Locate every Plasmodium parasite.
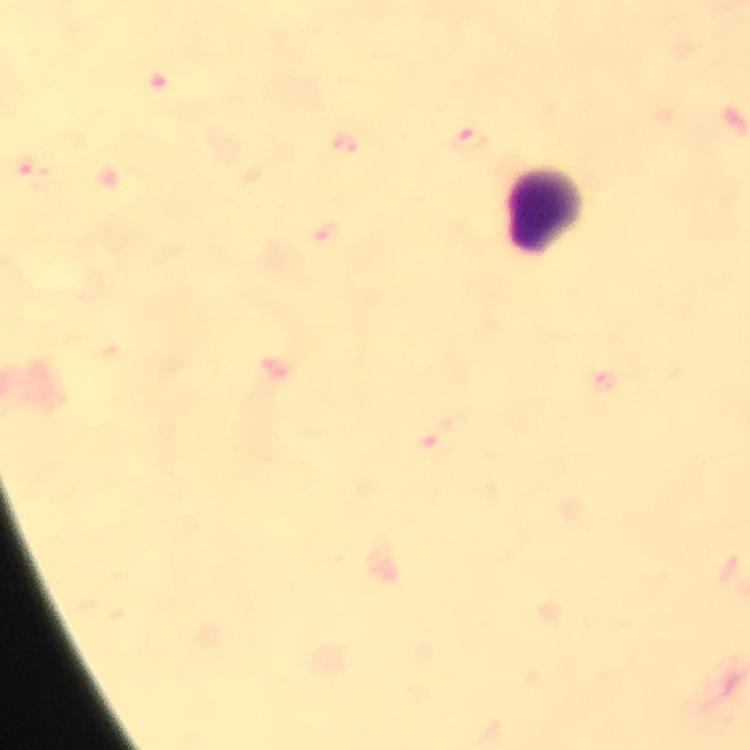

Approximate object centers, in pixels from the top-left corner.
Plasmodium parasites: (x=466, y=139), (x=331, y=238), (x=604, y=383).

Leukocyte locations: (x=547, y=210). Immersion oil applied. 100x magnification. Thick blood smear. From a malaria diagnostic workup. Photographed with a smartphone mounted on the microscope. Image is 750×750 pixels. Giemsa-stained preparation. Cropped region of a single field of view.